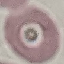
Summary:
  - Result: no malaria parasites detected
  - Preparation: thin smear
  - Stain: Giemsa
  - Capture: smartphone camera at the microscope eyepiece
  - Image type: cell patch, automatically extracted from a larger field of view and resized to 64 × 64 pixels